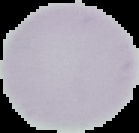

Summary:
  - Image size: 139×133 pixels
  - Malaria status: uninfected
  - Image type: segmented cell region with the area outside set to black
  - Preparation: thin blood film